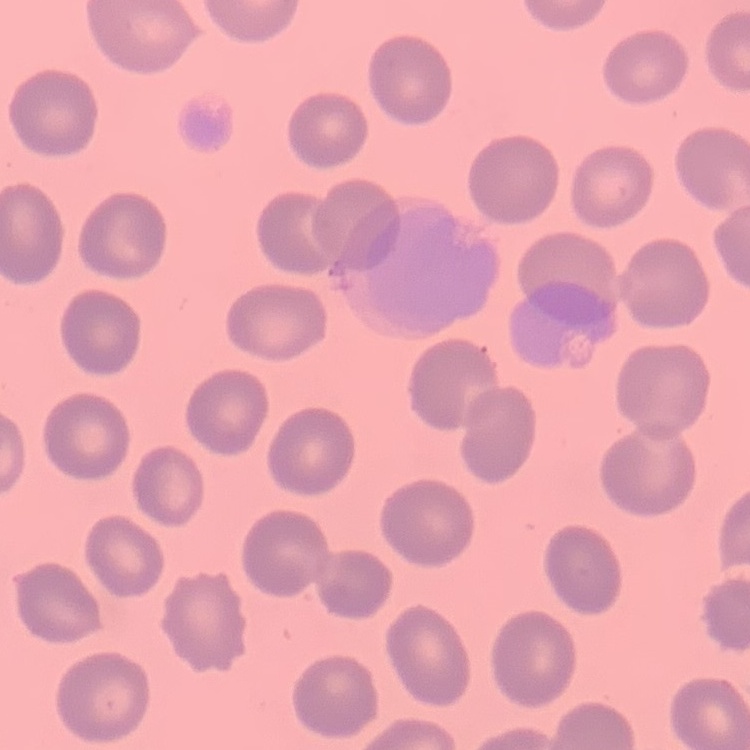
red_blood_cell_morphology: no rouleaux formation
preparation: thin blood film
image_type: square crop of a larger photomicrograph
stain: Field's or Giemsa